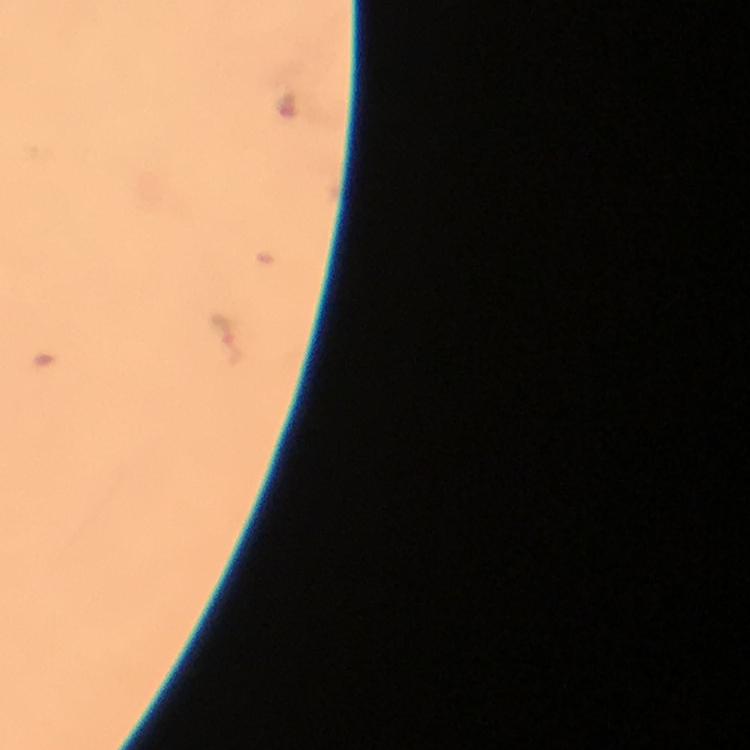

cropped from = one field of view
immersion oil = applied
malaria parasite locations = approximate centers as [x, y] in pixels: [226, 328]
capture = smartphone photograph through a microscope
image size = 750×750 pixels
context = from a diagnostic examination for malaria
preparation = thick smear
magnification = 100x
stain = Giemsa